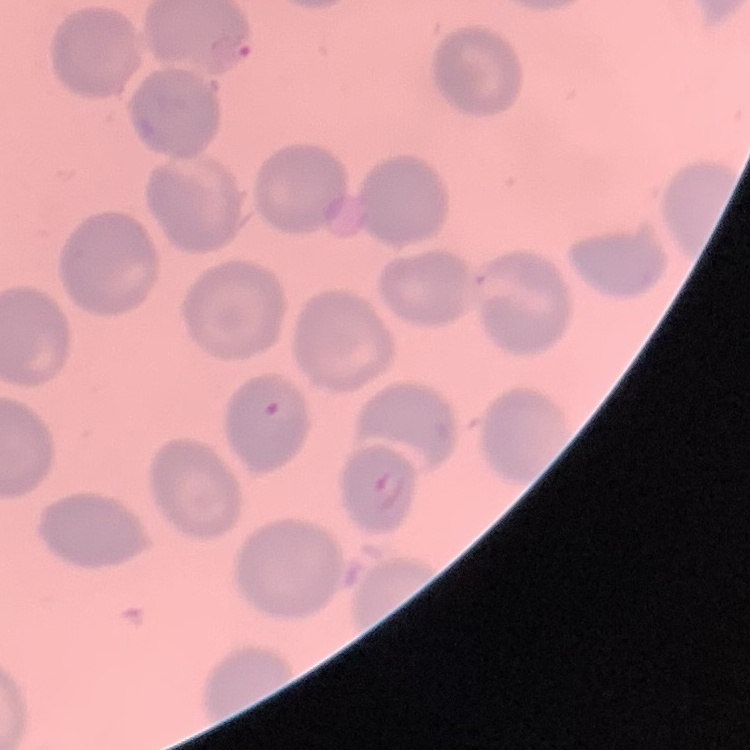

{
  "erythrocyte_morphology": "no rouleaux formation",
  "stain": "Field's or Giemsa",
  "preparation": "thin blood smear",
  "image_type": "square crop of a larger photomicrograph"
}